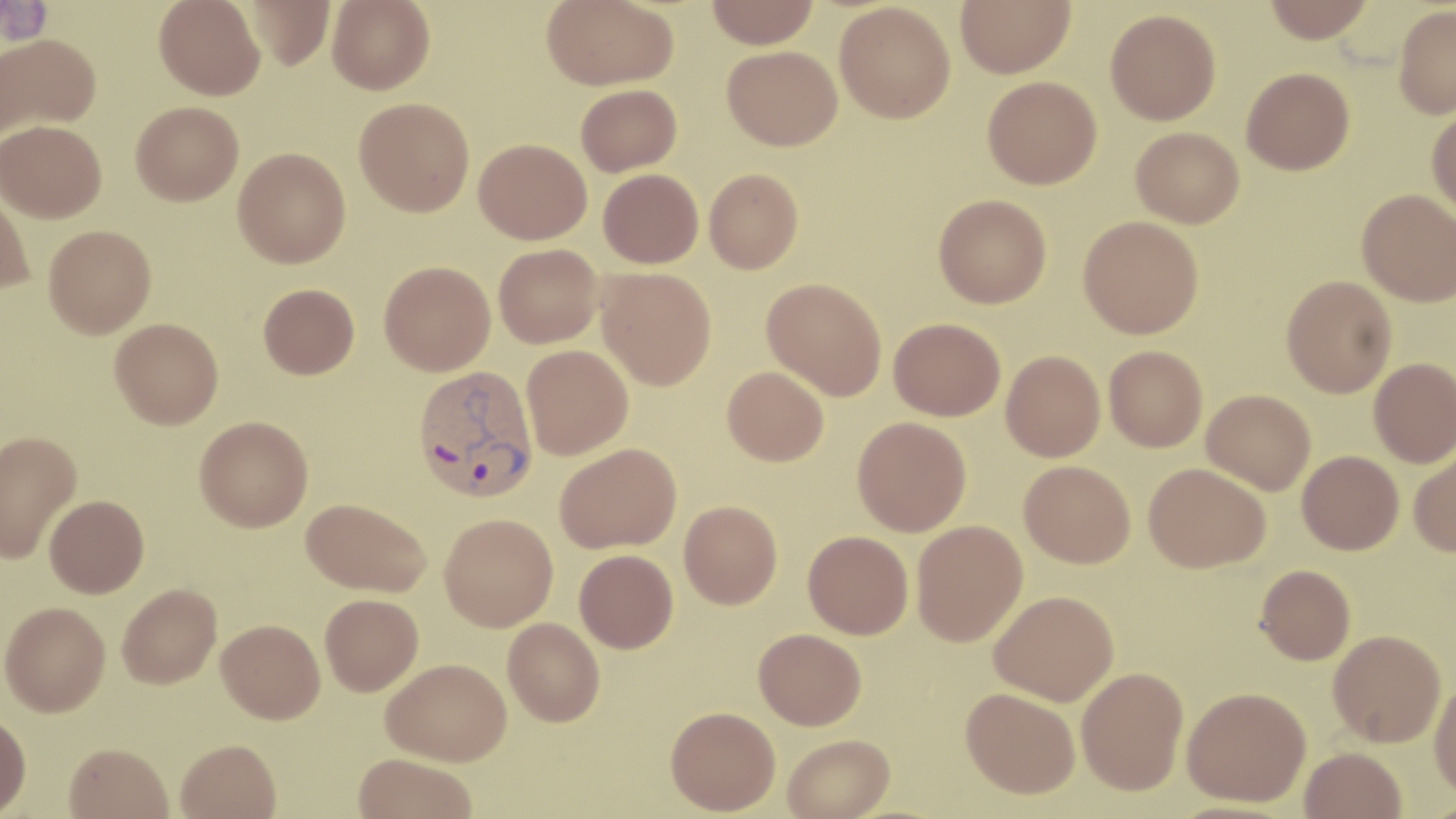
{
  "slide_level_diagnosis": "Plasmodium vivax",
  "field_of_view": "single",
  "image_size": "1456×819 pixels",
  "magnification": "1000x",
  "modality": "light microscopy",
  "plasmodium_vivax_infected_red_blood_cell_locations": "approximate bounding boxes as (x1,y1)-(x2,y2) corner pairs in pixels: (412,364)-(539,502)",
  "stain": "May-Grünwald-Giemsa",
  "uninfected_red_blood_cell_locations": "approximate bounding boxes as (x1,y1)-(x2,y2) corner pairs in pixels: (154,0)-(265,100), (244,0)-(336,70), (327,0)-(434,94), (542,0)-(680,90), (706,0)-(819,48), (955,0)-(1075,77), (1262,0)-(1375,42), (834,2)-(955,123), (1393,5)-(1456,118), (1105,8)-(1222,125), (1,33)-(101,139), (722,45)-(843,150), (1241,67)-(1355,175), (982,76)-(1102,189), (576,84)-(681,176), (354,96)-(475,216), (131,101)-(244,206), (1426,108)-(1456,218), (1,119)-(107,222), (1131,127)-(1244,227), (474,138)-(591,244), (233,146)-(351,267), (598,168)-(704,268), (704,168)-(803,274), (0,184)-(35,295), (1357,189)-(1456,306), (933,194)-(1051,308), (1078,215)-(1203,338), (43,224)-(156,338), (493,243)-(602,348), (379,261)-(495,375), (596,268)-(717,390), (1281,275)-(1396,398), (761,277)-(887,400), (258,283)-(359,379), (888,317)-(1006,420), (110,318)-(223,429), (521,344)-(634,459), (1104,345)-(1207,451), (1001,350)-(1105,461), (1369,357)-(1456,467), (722,366)-(829,466), (1202,389)-(1316,494), (194,415)-(313,532), (852,416)-(972,536), (0,429)-(82,565), (554,443)-(682,553), (1408,446)-(1456,556), (1297,450)-(1404,554), (1019,460)-(1135,568), (1143,463)-(1271,572), (44,495)-(149,598), (301,497)-(431,596), (679,500)-(782,609), (439,513)-(558,631), (911,520)-(1028,646), (803,530)-(914,639), (574,549)-(678,653), (1255,564)-(1355,664), (117,583)-(222,688), (989,589)-(1118,706), (320,593)-(424,696), (1,601)-(110,716), (503,618)-(605,726), (216,619)-(325,723), (754,628)-(866,730), (1328,630)-(1446,747), (382,658)-(512,765), (1077,666)-(1188,794), (1430,676)-(1456,801), (1183,686)-(1311,806), (961,687)-(1080,798), (665,706)-(781,815), (0,712)-(31,818), (782,734)-(894,819), (175,738)-(281,819), (63,742)-(174,819), (1300,747)-(1407,819), (354,753)-(477,819)",
  "preparation": "thin blood smear"
}